Report the malaria status of this cell.
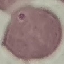
It is uninfected.

Summary:
  - Preparation: thin blood film
  - Capture: smartphone through the microscope eyepiece
  - Stain: Giemsa
  - Image type: cell patch, automatically extracted from a larger field of view and resized to 64 × 64 pixels